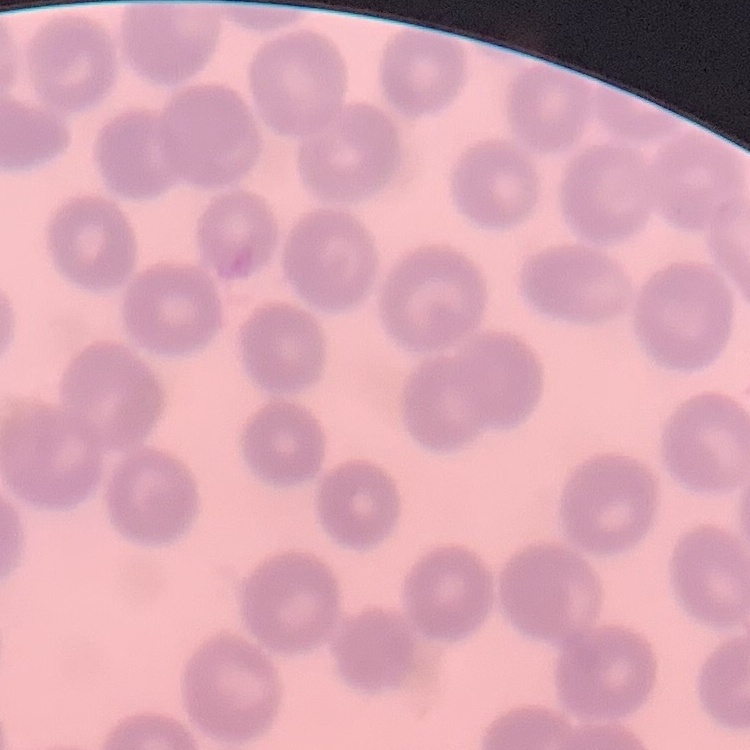
red blood cell morphology = no rouleaux formation
image type = square crop of a larger photomicrograph
preparation = thin peripheral smear
stain = Field's or Giemsa